State which parasite is depicted.
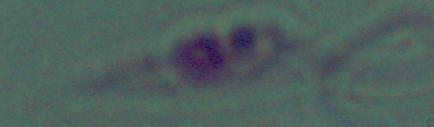

Leishmania.

Summary:
  - Magnification: 1000x
  - Modality: micrograph